State which parasite is depicted.
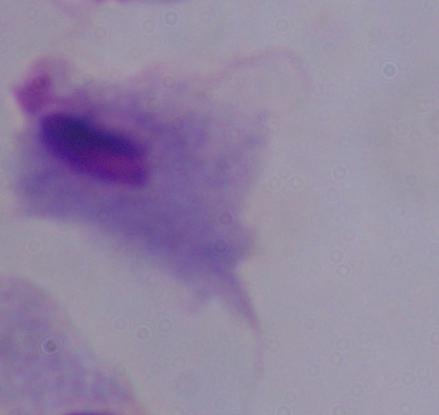

A trichomonad.

1000x magnification. Photomicrograph.